Name the blood parasite species.
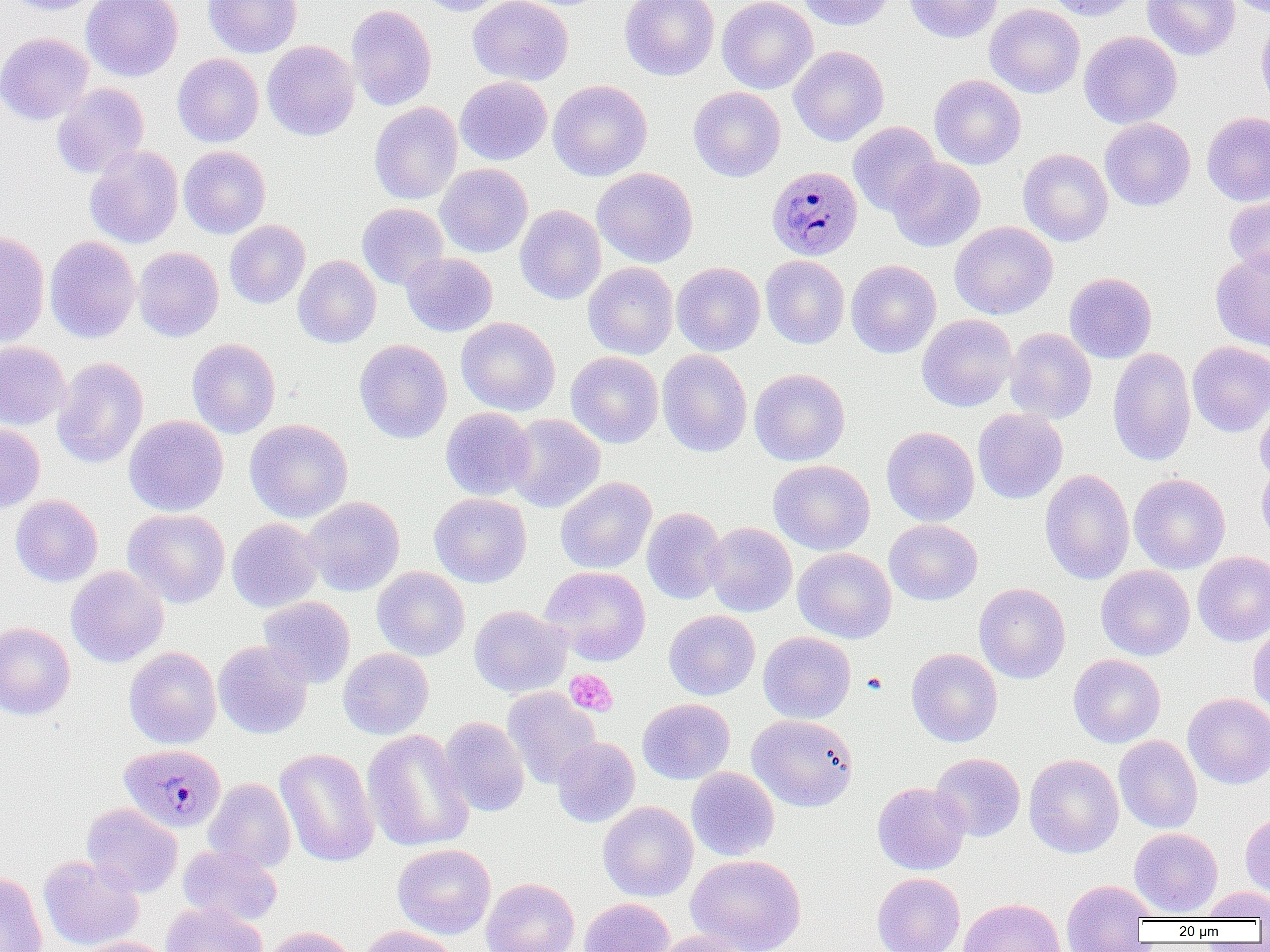
Plasmodium malariae.

Summary:
  - Coordinate format: approximate bounding boxes as (x1,y1)-(x2,y2) corner pairs in pixels
  - Plasmodium malariae-infected red blood cell locations: (766,165)-(862,261), (118,744)-(226,832)
  - Uninfected red blood cell locations: (6,0)-(103,15), (81,0)-(183,82), (203,0)-(302,58), (415,0)-(508,16), (468,0)-(573,86), (620,0)-(720,81), (717,0)-(817,94), (798,0)-(895,30), (903,0)-(1004,43), (1044,0)-(1140,21), (1142,0)-(1239,61), (346,4)-(437,111), (984,4)-(1085,98), (1256,12)-(1270,116), (1078,31)-(1182,129), (0,32)-(93,125), (261,40)-(360,141), (788,45)-(889,146), (172,53)-(263,147), (929,74)-(1026,170), (455,76)-(552,165), (548,80)-(652,181), (51,83)-(150,178), (688,87)-(786,182), (369,102)-(463,204), (1201,111)-(1270,206), (1100,118)-(1196,211), (848,122)-(941,216), (84,146)-(183,249), (178,146)-(271,238), (1018,148)-(1113,246), (887,157)-(986,252), (435,163)-(533,257), (593,167)-(698,267), (1225,195)-(1270,280), (357,203)-(448,290), (515,205)-(606,304), (224,220)-(310,309), (949,221)-(1058,319), (0,229)-(50,348), (44,236)-(140,344), (133,247)-(224,342), (1211,249)-(1270,351), (401,252)-(497,337), (293,255)-(381,349), (760,255)-(849,349), (846,259)-(941,359), (583,262)-(678,359), (672,262)-(765,356), (1064,272)-(1157,363), (917,313)-(1017,412), (456,317)-(560,415), (1004,327)-(1097,423), (187,338)-(280,438), (354,339)-(452,443), (0,341)-(70,429), (1187,341)-(1270,437), (1107,347)-(1196,466), (657,350)-(753,457), (565,351)-(664,448), (52,357)-(149,469), (749,368)-(850,466), (1255,398)-(1270,485), (440,407)-(536,500), (972,408)-(1068,504), (504,414)-(606,513), (124,415)-(228,516), (244,419)-(353,523), (0,423)-(45,513), (881,426)-(979,526), (768,460)-(875,555), (1257,462)-(1270,549), (1040,468)-(1135,585), (1129,473)-(1230,573), (555,477)-(656,574), (429,493)-(531,587), (10,494)-(103,587), (302,496)-(405,596), (642,507)-(728,605), (123,509)-(230,608), (227,518)-(324,612), (884,519)-(982,605), (703,522)-(797,617), (793,548)-(896,643), (1192,551)-(1270,646), (1096,565)-(1195,660), (66,566)-(168,668), (372,566)-(470,661), (539,566)-(651,665), (974,583)-(1071,684), (258,596)-(355,688), (469,605)-(571,697), (663,610)-(760,700), (1248,621)-(1270,716), (0,622)-(75,720), (758,631)-(856,723), (213,641)-(313,739), (124,647)-(221,749), (337,648)-(434,739), (906,648)-(1003,747), (1068,654)-(1166,748), (502,688)-(601,788), (1183,693)-(1270,789), (637,698)-(735,784), (747,714)-(858,812), (439,716)-(529,817), (362,729)-(474,852), (1114,735)-(1203,833), (551,736)-(640,827), (275,747)-(379,868), (931,753)-(1025,842), (1024,754)-(1124,858), (686,767)-(780,861), (204,778)-(296,873), (872,782)-(970,875), (598,801)-(698,902), (82,803)-(183,897), (1240,810)-(1270,900), (1129,827)-(1222,917), (177,844)-(282,926), (392,844)-(496,939), (686,854)-(806,952), (38,855)-(144,951), (0,873)-(47,952), (872,873)-(965,952), (481,877)-(580,952), (1061,879)-(1154,951), (1200,886)-(1270,921), (579,897)-(676,952), (958,897)-(1066,952), (161,902)-(267,952), (358,925)-(461,952), (262,926)-(358,952), (651,930)-(748,952), (74,937)-(174,952)
  - Platelet locations: (565,669)-(617,717), (862,672)-(887,694)
  - Image size: 1270×952 pixels
  - Field of view: one of a larger specimen
  - Magnification: 1000x
  - Modality: optical microscopy
  - Preparation: thin blood film